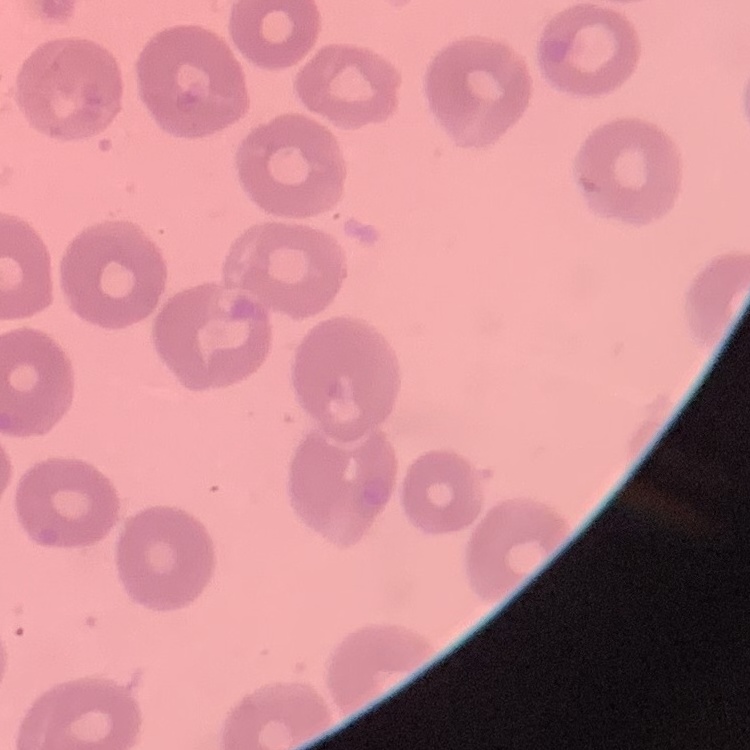

The erythrocytes exhibit no rouleaux formation. Stained with either Field's or Giemsa. Thin blood film. Square crop of a larger photomicrograph.